Report the malaria status of this cell.
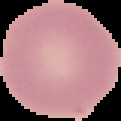
Uninfected.

Summary:
  - Image size: 121×121 pixels
  - Image type: segmented cell region with the area outside set to black
  - Preparation: thin blood smear